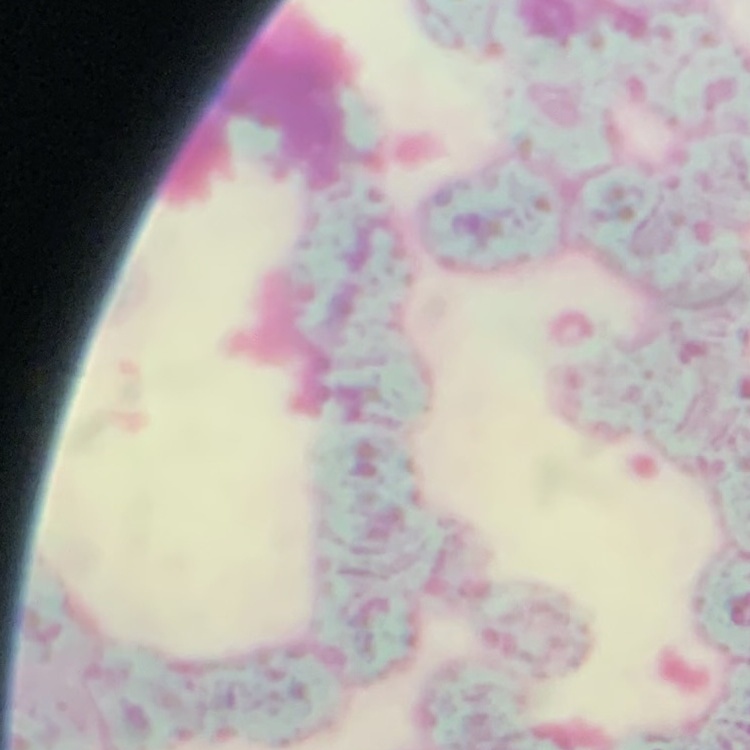
The red blood cells show rouleaux formation. Field's or Giemsa stain. Thin blood smear. One tile cut from a larger photomicrograph.